Outline each blood parasite and name the species.
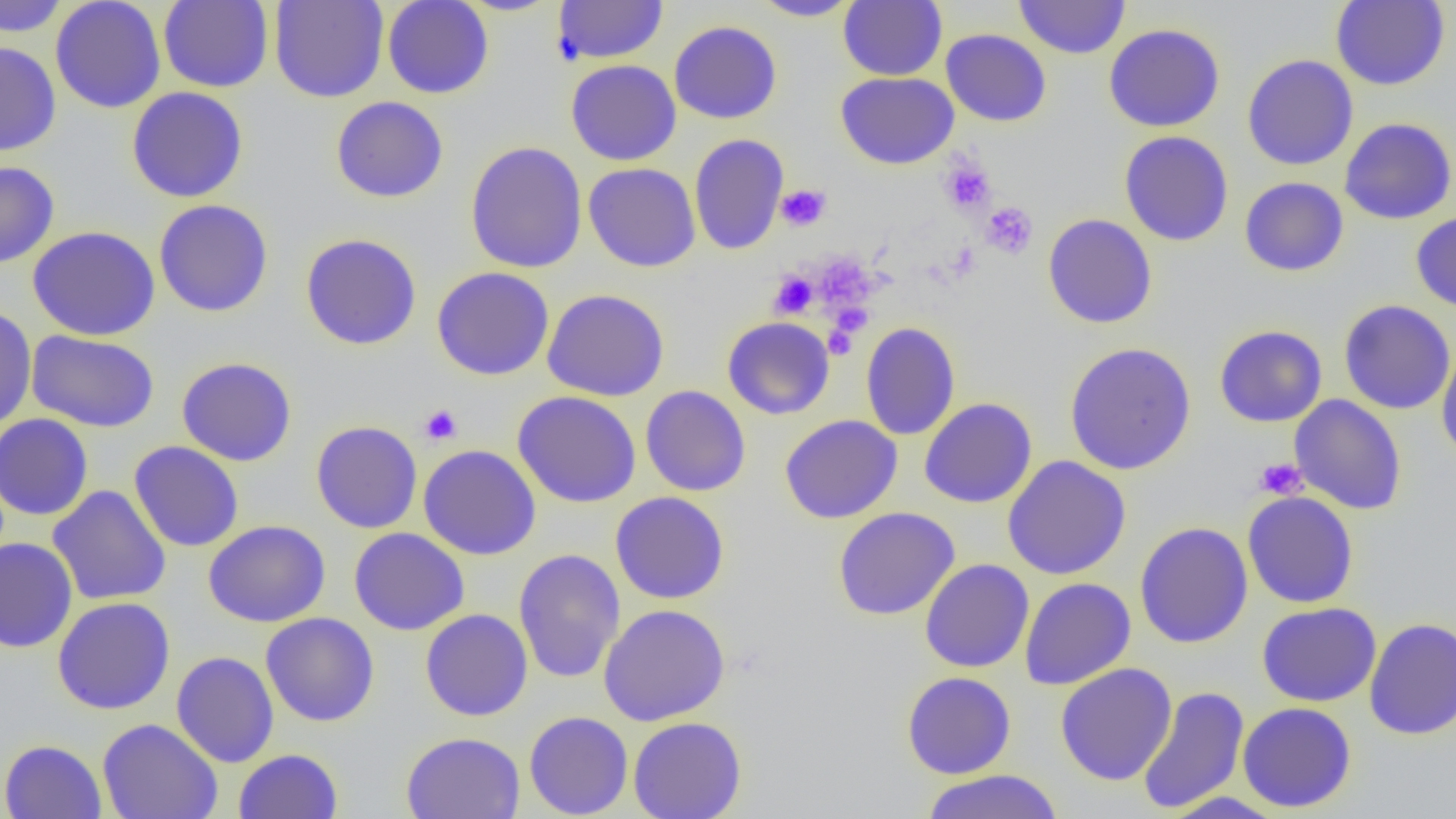

No blood parasites observed.

slide-level diagnosis = no evidence of blood parasites
magnification = 1000x
image size = 1456×819 pixels
modality = optical microscopy
preparation = thin blood smear
field of view = single
uninfected red blood cell locations = approximate bounding boxes as named x1/y1/x2/y2 corners in pixels: (x1=0, y1=0, x2=68, y2=37), (x1=50, y1=0, x2=166, y2=114), (x1=269, y1=0, x2=389, y2=103), (x1=382, y1=0, x2=494, y2=99), (x1=749, y1=0, x2=862, y2=21), (x1=1014, y1=0, x2=1130, y2=59), (x1=1331, y1=0, x2=1450, y2=90), (x1=158, y1=1, x2=274, y2=92), (x1=553, y1=1, x2=669, y2=64), (x1=838, y1=1, x2=947, y2=81), (x1=669, y1=20, x2=782, y2=124), (x1=1103, y1=23, x2=1225, y2=132), (x1=941, y1=29, x2=1052, y2=127), (x1=0, y1=41, x2=61, y2=156), (x1=1242, y1=54, x2=1358, y2=171), (x1=566, y1=59, x2=682, y2=166), (x1=835, y1=72, x2=959, y2=169), (x1=126, y1=86, x2=248, y2=203), (x1=331, y1=96, x2=448, y2=203), (x1=1339, y1=117, x2=1456, y2=224), (x1=1119, y1=131, x2=1234, y2=246), (x1=689, y1=133, x2=789, y2=255), (x1=465, y1=142, x2=588, y2=274), (x1=0, y1=160, x2=59, y2=269), (x1=583, y1=162, x2=701, y2=272), (x1=1239, y1=177, x2=1349, y2=276), (x1=153, y1=199, x2=274, y2=317), (x1=1411, y1=211, x2=1456, y2=313), (x1=1043, y1=213, x2=1157, y2=329), (x1=27, y1=225, x2=160, y2=340), (x1=300, y1=233, x2=422, y2=350), (x1=431, y1=266, x2=554, y2=381), (x1=542, y1=288, x2=670, y2=401), (x1=1339, y1=299, x2=1455, y2=415), (x1=0, y1=305, x2=37, y2=431), (x1=722, y1=316, x2=835, y2=420), (x1=860, y1=322, x2=961, y2=441), (x1=1214, y1=325, x2=1327, y2=427), (x1=26, y1=329, x2=160, y2=432), (x1=1436, y1=339, x2=1456, y2=466), (x1=1064, y1=342, x2=1196, y2=475), (x1=176, y1=356, x2=297, y2=466), (x1=640, y1=385, x2=751, y2=497), (x1=513, y1=391, x2=642, y2=508), (x1=1289, y1=395, x2=1407, y2=515), (x1=919, y1=397, x2=1037, y2=509), (x1=0, y1=413, x2=94, y2=521), (x1=780, y1=415, x2=902, y2=524), (x1=311, y1=420, x2=422, y2=534), (x1=129, y1=440, x2=244, y2=552), (x1=418, y1=444, x2=541, y2=560), (x1=1002, y1=455, x2=1131, y2=580), (x1=47, y1=485, x2=171, y2=606), (x1=1242, y1=490, x2=1359, y2=608), (x1=610, y1=491, x2=730, y2=605), (x1=832, y1=506, x2=960, y2=620), (x1=203, y1=520, x2=330, y2=627), (x1=1135, y1=521, x2=1253, y2=649), (x1=349, y1=527, x2=469, y2=635), (x1=0, y1=538, x2=78, y2=652), (x1=513, y1=548, x2=626, y2=684), (x1=920, y1=558, x2=1034, y2=673), (x1=1020, y1=577, x2=1136, y2=690), (x1=52, y1=597, x2=175, y2=714), (x1=1256, y1=602, x2=1381, y2=707), (x1=598, y1=604, x2=730, y2=726), (x1=420, y1=608, x2=533, y2=721), (x1=260, y1=612, x2=380, y2=727), (x1=1364, y1=617, x2=1456, y2=740), (x1=171, y1=651, x2=280, y2=767), (x1=1055, y1=663, x2=1177, y2=785), (x1=901, y1=671, x2=1017, y2=779), (x1=1136, y1=685, x2=1250, y2=814), (x1=1237, y1=702, x2=1356, y2=812), (x1=523, y1=711, x2=633, y2=818), (x1=628, y1=716, x2=747, y2=819), (x1=98, y1=718, x2=223, y2=819), (x1=401, y1=731, x2=525, y2=819), (x1=1, y1=739, x2=107, y2=818), (x1=233, y1=749, x2=343, y2=819), (x1=920, y1=769, x2=1064, y2=819), (x1=1160, y1=791, x2=1287, y2=819)
platelet locations = approximate bounding boxes as named x1/y1/x2/y2 corners in pixels: (x1=939, y1=157, x2=996, y2=215), (x1=776, y1=184, x2=831, y2=231), (x1=980, y1=201, x2=1038, y2=258), (x1=814, y1=254, x2=879, y2=314), (x1=769, y1=271, x2=818, y2=318), (x1=829, y1=302, x2=872, y2=338), (x1=824, y1=322, x2=861, y2=359), (x1=419, y1=404, x2=463, y2=446), (x1=1254, y1=457, x2=1307, y2=499)